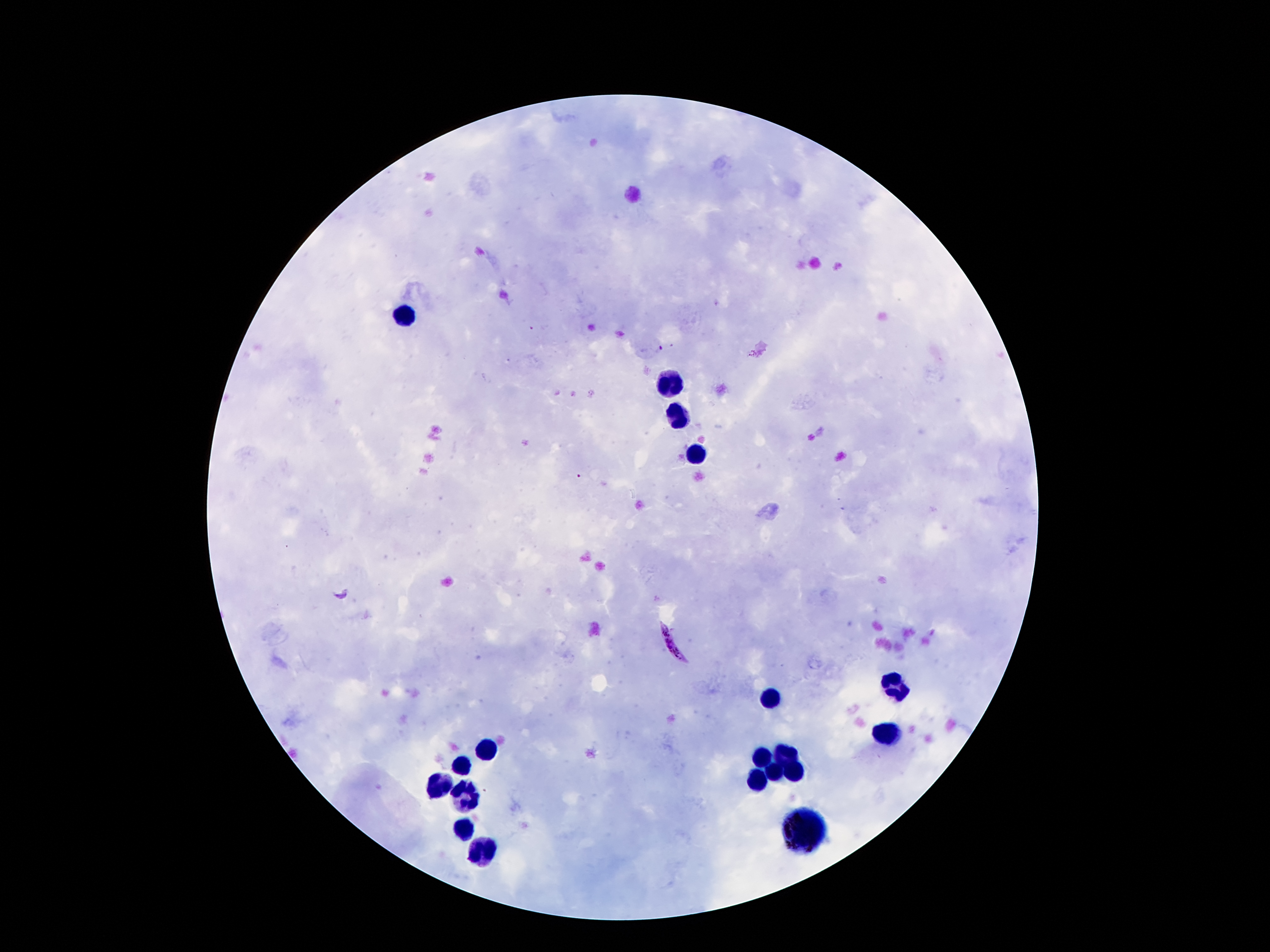

Approximate centers as {x, y} in pixels.
Summary:
  - Leukocyte locations: {409, 315}, {667, 382}, {680, 417}, {696, 454}, {895, 683}, {772, 696}, {891, 733}, {489, 748}, {783, 753}, {762, 758}, {465, 765}, {795, 768}, {775, 773}, {757, 782}, {442, 783}, {467, 797}, {460, 829}, {801, 829}, {483, 853}
  - Plasmodium parasite locations: {662, 349}, {580, 476}, {671, 645}
  - Preparation: thick peripheral-blood smear
  - Magnification: 100x
  - Field of view: single
  - Patient malaria status: infected with Plasmodium falciparum
  - Image size: 1270×952 pixels
  - Stain: Giemsa
  - Capture: smartphone through the microscope eyepiece